State which parasite is depicted.
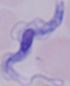
A trypanosome.

Photomicrograph. Captured at 1000x magnification.